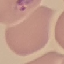

Result: malaria parasites identified. Acquired by smartphone through the microscope eyepiece. Thin blood film. Cell patch, automatically extracted from a larger field of view and resized to 64 × 64 pixels. Giemsa stain.